Point out each Plasmodium parasite.
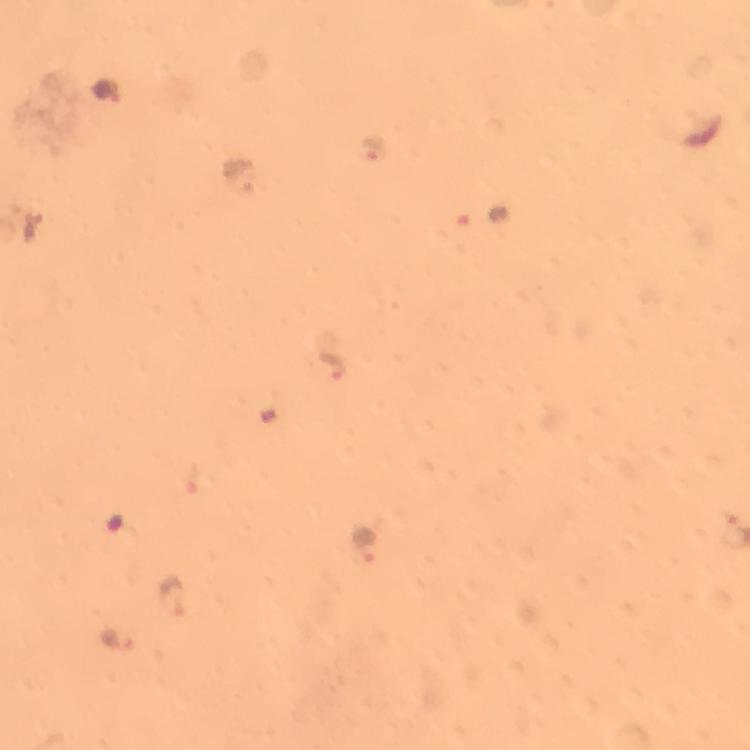
Approximate object centers, in pixels from the top-left corner.
Plasmodium parasites: (x=374, y=150), (x=235, y=176), (x=32, y=228), (x=332, y=366), (x=364, y=543), (x=171, y=595), (x=120, y=640).

Summary:
  - Capture: smartphone photograph through a microscope
  - Stain: Giemsa
  - Magnification: 100x
  - Context: from a malaria diagnostic workup
  - Preparation: thick blood film
  - Cropped from: one field of view
  - Image size: 750×750 pixels
  - Immersion oil: used